Locate platelets.
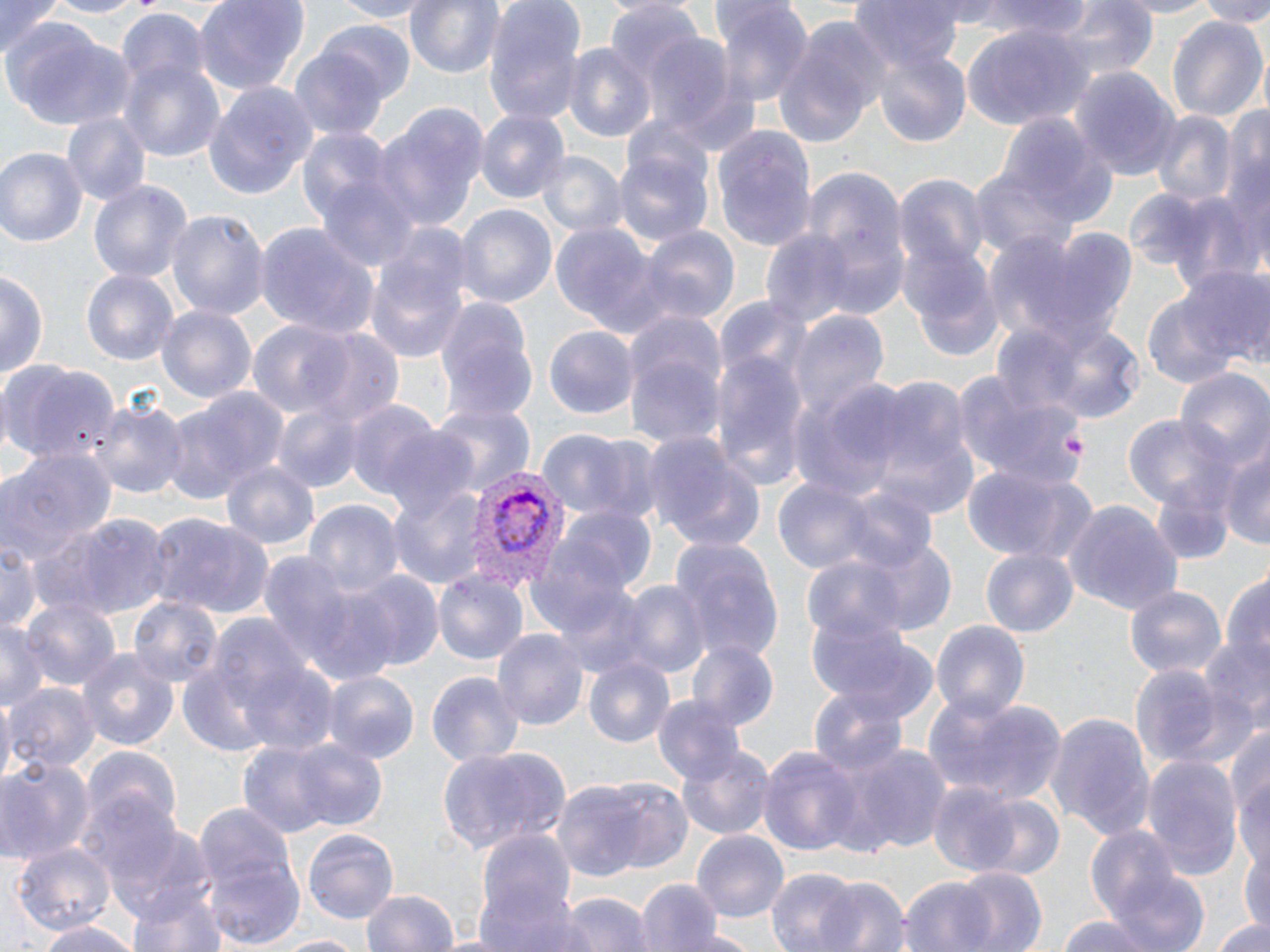
Approximate bounding boxes as (x1, y1, x2, y2) in pixels.
Platelets: (1062, 435, 1084, 455).

slide_level_diagnosis: Plasmodium vivax
field_of_view: single
preparation: thin blood film
image_size: 1270×952 pixels
magnification: 1000x
plasmodium_vivax_infected_red_blood_cell_locations: 'approximate bounding boxes as (x1, y1, x2, y2) in pixels: (462, 466, 565, 589)'
modality: optical microscopy
uninfected_red_blood_cell_locations: 'approximate bounding boxes as (x1, y1, x2, y2) in pixels: (1, 0, 63, 55), (40, 0, 155, 20), (191, 0, 312, 95), (319, 0, 434, 21), (405, 0, 502, 82), (483, 0, 585, 126), (850, 0, 969, 76), (974, 0, 1094, 41), (1102, 0, 1228, 19), (1192, 0, 1270, 25), (717, 2, 813, 111), (1048, 2, 1160, 82), (605, 3, 710, 108), (115, 11, 209, 99), (1167, 13, 1268, 125), (771, 19, 888, 150), (321, 20, 416, 102), (7, 25, 134, 129), (960, 25, 1090, 133), (641, 32, 742, 139), (869, 41, 972, 146), (563, 42, 657, 147), (290, 47, 390, 140), (119, 58, 224, 161), (1072, 68, 1181, 180), (201, 81, 317, 201), (374, 105, 486, 233), (475, 108, 569, 203), (61, 110, 151, 205), (1154, 111, 1237, 205), (996, 114, 1118, 228), (713, 126, 815, 253), (1223, 127, 1270, 274), (612, 144, 715, 252), (0, 148, 86, 251), (536, 153, 625, 242), (792, 164, 911, 316), (972, 168, 1078, 262), (895, 173, 988, 271), (88, 180, 190, 288), (1152, 187, 1258, 290), (453, 203, 558, 310), (168, 209, 269, 327), (549, 223, 664, 339), (252, 224, 376, 341), (1006, 225, 1139, 350), (362, 226, 471, 363), (638, 227, 739, 327), (761, 230, 859, 329), (903, 244, 1004, 362), (1180, 266, 1270, 364), (0, 268, 47, 388), (81, 268, 178, 366), (1142, 293, 1240, 391), (433, 296, 537, 423), (157, 304, 257, 406), (786, 310, 886, 421), (622, 312, 726, 452), (1008, 319, 1151, 425), (248, 321, 354, 418), (544, 327, 637, 418), (307, 329, 404, 430), (710, 346, 807, 486), (0, 360, 119, 470), (954, 368, 1083, 488), (1176, 369, 1270, 476), (788, 378, 910, 502), (861, 378, 977, 517), (166, 384, 288, 502), (348, 397, 438, 498), (91, 398, 188, 501), (272, 403, 367, 493), (433, 403, 534, 498), (1123, 416, 1228, 507), (378, 425, 482, 519), (535, 430, 633, 515), (646, 432, 767, 553), (1, 443, 117, 567), (1220, 443, 1270, 553), (221, 461, 319, 548), (961, 465, 1097, 566), (1149, 473, 1241, 566), (772, 480, 878, 574), (386, 481, 490, 593), (831, 485, 939, 576), (304, 497, 403, 603), (1063, 499, 1178, 616), (559, 506, 660, 598), (147, 511, 276, 616), (42, 514, 171, 620), (668, 538, 786, 669), (842, 539, 959, 636), (0, 541, 47, 634), (981, 546, 1079, 638), (259, 552, 360, 668), (801, 554, 911, 647), (1219, 566, 1270, 683), (433, 568, 529, 667), (347, 573, 443, 670), (619, 581, 708, 677), (1123, 583, 1228, 680), (21, 598, 120, 697), (131, 598, 221, 692), (0, 618, 48, 713), (930, 620, 1030, 723), (811, 623, 940, 723), (493, 627, 588, 730), (1198, 633, 1270, 724), (688, 639, 778, 731), (76, 647, 180, 749), (581, 658, 675, 749), (241, 661, 338, 759), (1129, 665, 1225, 768), (424, 670, 526, 766), (324, 671, 418, 764), (6, 681, 100, 776), (810, 689, 910, 780), (925, 693, 1070, 806), (654, 694, 745, 785), (0, 696, 16, 786), (1047, 714, 1157, 841), (1225, 718, 1270, 850), (246, 736, 393, 837), (436, 742, 572, 856), (832, 743, 953, 857), (676, 744, 777, 841), (83, 745, 183, 844), (757, 745, 864, 855), (1140, 754, 1243, 879), (0, 757, 95, 867), (549, 779, 663, 885), (927, 782, 1023, 877), (970, 794, 1066, 881), (192, 802, 301, 949), (92, 806, 214, 924), (1083, 823, 1197, 940), (302, 829, 398, 924), (692, 831, 788, 919), (472, 832, 580, 952), (12, 843, 115, 939), (1242, 851, 1270, 934), (949, 866, 1048, 952), (1108, 867, 1210, 952), (768, 868, 858, 951), (815, 873, 911, 952), (898, 874, 1002, 952), (125, 875, 232, 952), (636, 879, 722, 952), (357, 889, 460, 952), (553, 893, 651, 952), (1057, 915, 1158, 952), (1216, 916, 1270, 951), (34, 922, 143, 952), (677, 929, 763, 952), (269, 933, 366, 952)'
stain: May-Grünwald-Giemsa